Locate every malaria parasite.
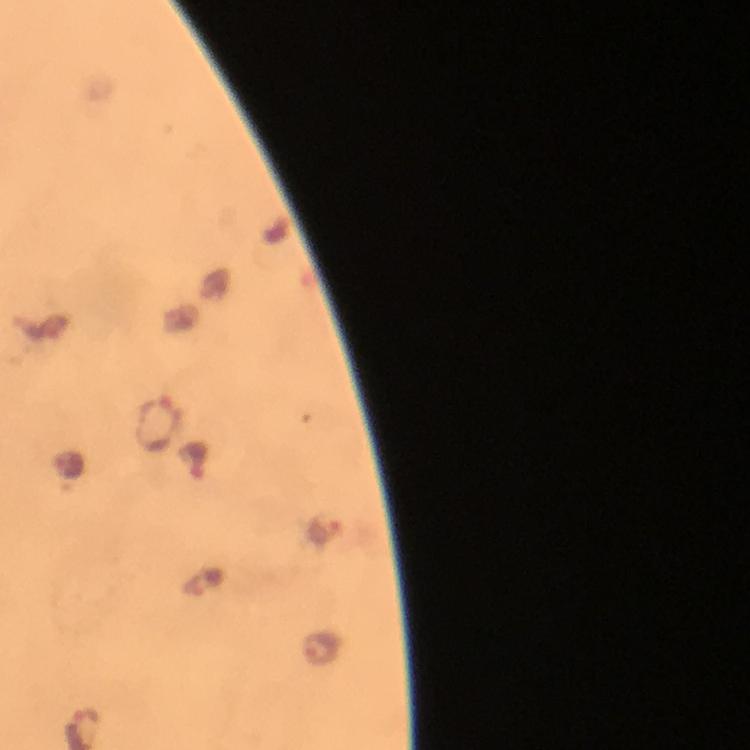
Approximate centers as [x, y] in pixels.
Malaria parasites: [159, 423], [199, 460], [324, 530], [323, 649].

Summary:
  - Cropped from: a single field of view
  - Stain: Giemsa
  - Image size: 750×750 pixels
  - Context: from a malaria diagnostic workup
  - Magnification: 100x
  - Capture: smartphone photograph through a microscope
  - Immersion oil: applied
  - Preparation: thick smear